Locate and identify every blood parasite.
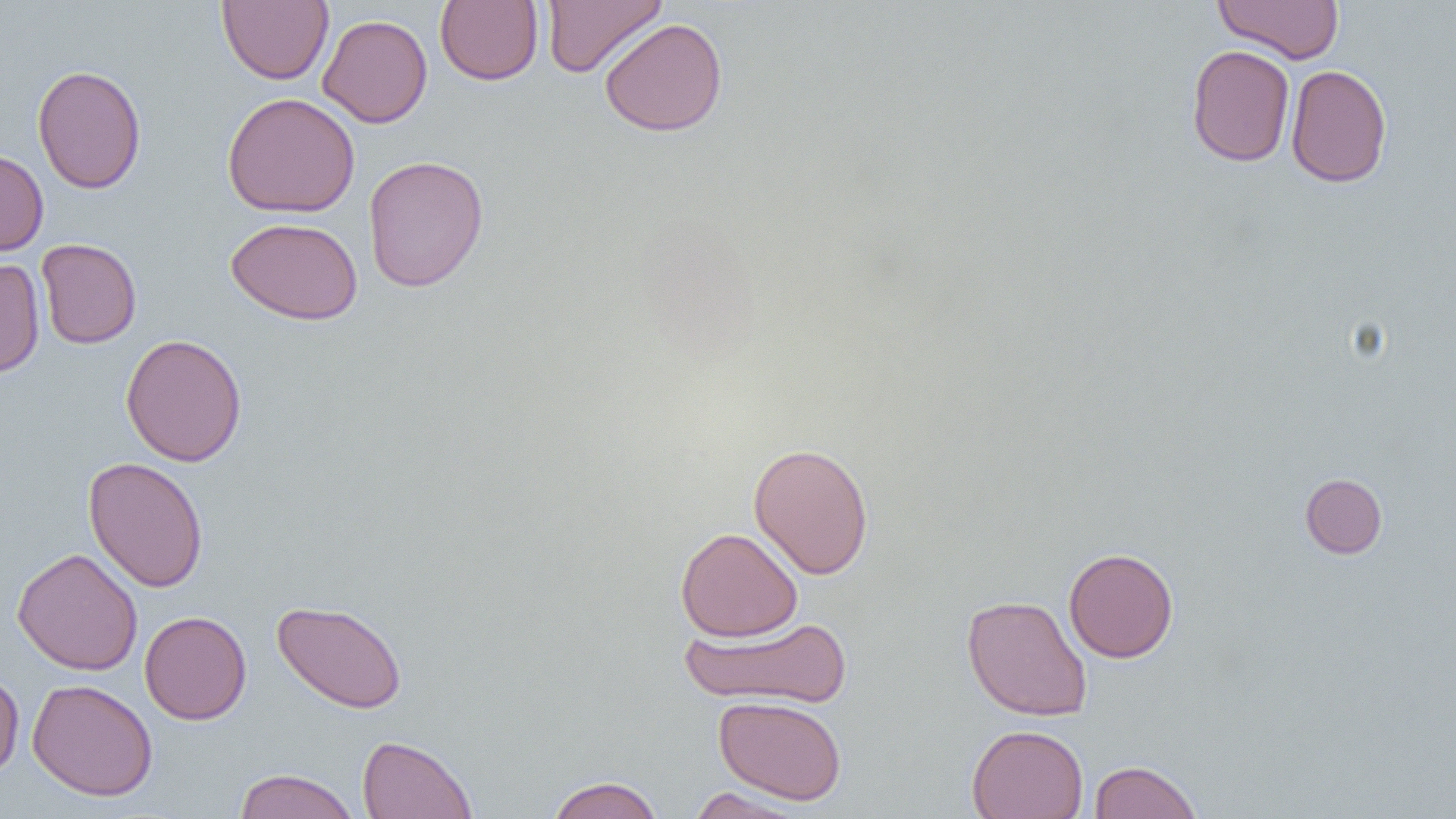
No blood parasites seen.

slide-level diagnosis = no evidence of blood parasites
uninfected red blood cell locations = approximate bounding boxes as [x1, y1, x2, y2] in pixels: [217, 0, 333, 85], [435, 0, 543, 86], [542, 0, 666, 77], [1213, 0, 1345, 64], [317, 14, 433, 128], [599, 18, 728, 137], [1186, 44, 1295, 167], [32, 63, 146, 194], [1286, 63, 1392, 188], [223, 92, 360, 218], [0, 148, 49, 256], [363, 154, 489, 292], [225, 217, 363, 325], [37, 238, 142, 349], [0, 259, 45, 378], [120, 333, 248, 467], [748, 442, 874, 580], [83, 456, 208, 593], [1299, 473, 1387, 559], [675, 527, 803, 642], [12, 547, 143, 675], [1063, 547, 1179, 663], [962, 594, 1093, 722], [271, 599, 408, 714], [139, 611, 252, 725], [681, 615, 851, 709], [0, 669, 24, 779], [27, 678, 158, 801], [713, 695, 847, 805], [966, 724, 1089, 819], [357, 734, 478, 819], [1088, 759, 1202, 819], [233, 768, 360, 819], [545, 776, 664, 819], [685, 787, 811, 819]
field of view = one of a larger specimen
preparation = thin blood smear
modality = light microscopy
magnification = 1000x
image size = 1456×819 pixels